Identify the parasite.
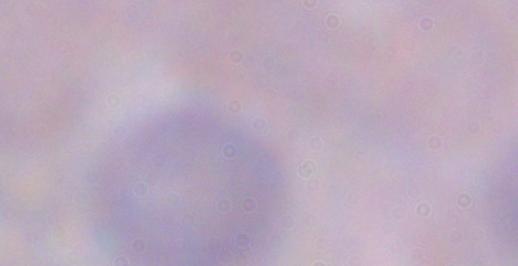

This is a trypanosome.

magnification: 1000x
modality: micrograph